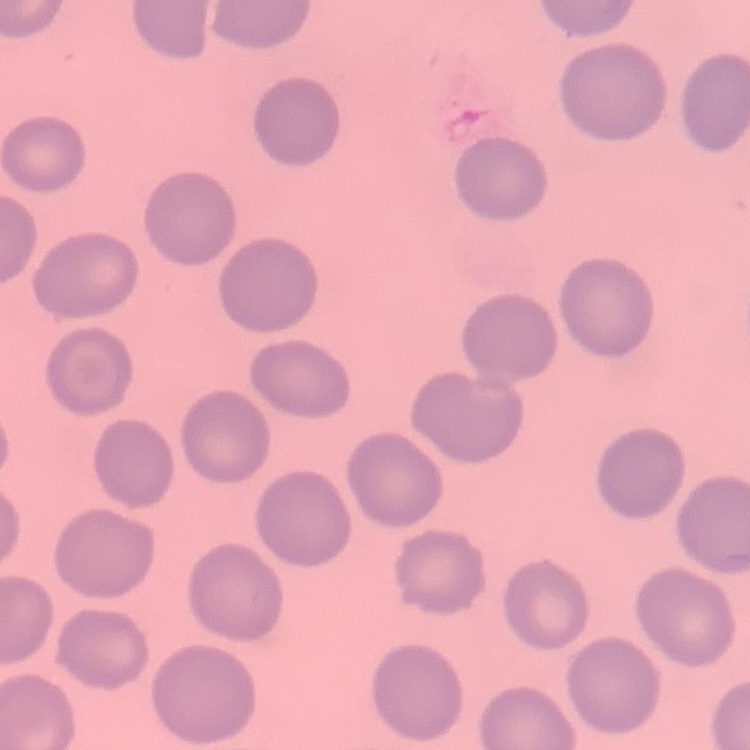

The erythrocytes show no rouleaux formation. Thin blood smear. Field's or Giemsa stain. One tile cut from a larger photomicrograph.